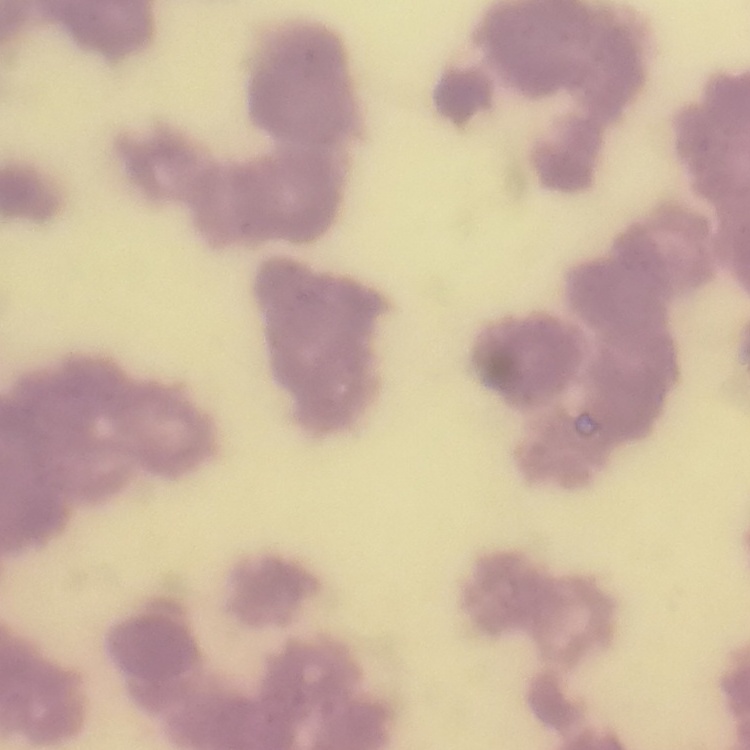
The erythrocytes exhibit rouleaux formation. One tile cut from a larger photomicrograph. Thin blood smear. Stained with either Field's or Giemsa.